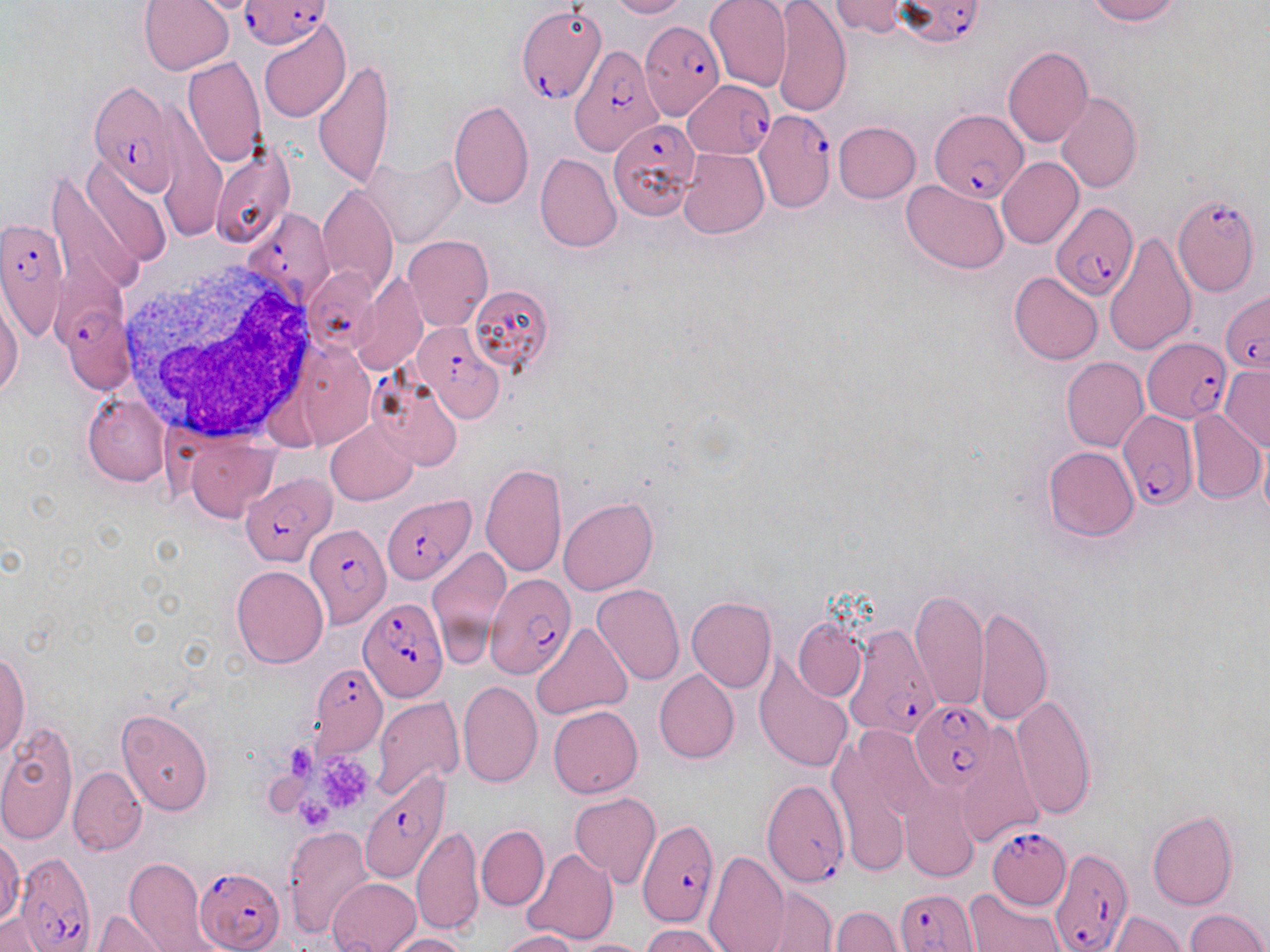
Approximate bounding boxes as (x1, y1, x2, y2) in pixels. Platelet locations: (288, 744, 313, 779), (313, 755, 374, 810), (294, 797, 336, 829). Uninfected red blood cell locations: (138, 0, 235, 75), (605, 0, 688, 19), (705, 0, 792, 91), (772, 0, 851, 117), (829, 0, 913, 37), (1084, 0, 1183, 25), (258, 19, 350, 124), (1002, 44, 1094, 147), (182, 56, 267, 168), (314, 59, 395, 190), (1055, 91, 1142, 194), (448, 99, 534, 209), (833, 121, 920, 203), (208, 144, 296, 250), (678, 148, 769, 239), (535, 153, 622, 253), (363, 155, 464, 248), (997, 156, 1083, 249), (50, 160, 164, 290), (902, 179, 1009, 274), (317, 185, 397, 298), (1104, 232, 1197, 356), (403, 235, 494, 331), (1008, 271, 1103, 366), (352, 275, 427, 376), (468, 283, 556, 375), (0, 291, 23, 398), (1060, 357, 1148, 452), (1220, 366, 1269, 450), (83, 392, 170, 486), (1188, 409, 1266, 503), (325, 421, 417, 506), (186, 436, 278, 521), (1259, 441, 1270, 525), (1043, 445, 1138, 541), (480, 461, 568, 578), (559, 497, 657, 596), (425, 544, 512, 664), (231, 564, 329, 668), (593, 583, 685, 686), (909, 587, 987, 712), (687, 597, 777, 693), (974, 604, 1052, 727), (794, 618, 867, 701), (531, 622, 632, 720), (0, 653, 30, 758), (755, 659, 853, 772), (655, 669, 738, 764), (458, 680, 542, 788), (1012, 695, 1096, 821), (372, 697, 464, 800), (548, 705, 643, 798), (116, 708, 214, 816), (0, 720, 78, 847), (955, 728, 1043, 848), (828, 732, 918, 876), (68, 766, 146, 854), (899, 789, 980, 881), (569, 792, 660, 888), (1147, 810, 1238, 910), (411, 825, 484, 936), (477, 825, 548, 910), (282, 826, 372, 938), (0, 838, 23, 926), (522, 848, 618, 944), (704, 850, 790, 952), (125, 857, 216, 952), (328, 878, 421, 952), (757, 886, 838, 952), (965, 886, 1065, 951), (828, 906, 903, 952), (1185, 908, 1268, 952), (91, 910, 171, 952), (1107, 912, 1184, 952), (1, 914, 49, 951), (639, 924, 730, 952), (495, 930, 577, 951), (387, 932, 472, 952), (563, 939, 651, 952). White blood cell locations: (117, 260, 324, 445). Plasmodium falciparum-infected red blood cell locations: (239, 0, 330, 50), (894, 0, 985, 46), (515, 4, 606, 105), (639, 21, 723, 122), (570, 46, 661, 156), (89, 79, 183, 195), (682, 80, 774, 158), (930, 107, 1027, 203), (754, 110, 836, 212), (608, 118, 697, 218), (1173, 194, 1261, 296), (1051, 200, 1138, 298), (241, 208, 336, 309), (0, 215, 70, 341), (1220, 291, 1270, 373), (62, 305, 138, 394), (413, 322, 504, 420), (1142, 337, 1232, 423), (369, 371, 463, 472), (1117, 412, 1197, 509), (240, 470, 335, 566), (383, 494, 475, 585), (304, 522, 390, 629), (484, 572, 573, 679), (358, 597, 447, 704), (842, 624, 944, 742), (308, 662, 388, 757), (910, 700, 998, 793), (358, 767, 452, 888), (764, 781, 848, 887), (638, 820, 720, 929), (984, 826, 1069, 911), (1051, 848, 1132, 952), (15, 851, 96, 947), (195, 866, 285, 952), (893, 886, 981, 951). Slide-level diagnosis: Plasmodium falciparum. Single field of view. Image is 1270×952 pixels. May-Grünwald-Giemsa stain. Thin blood film. Light microscopy. Captured at 1000x magnification.